Classify this cell by malaria status.
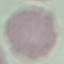

It is uninfected.

{
  "preparation": "thin blood smear",
  "stain": "Giemsa",
  "image_type": "automatically extracted cell patch, resized to 64 × 64 pixels",
  "capture": "smartphone through the microscope eyepiece"
}